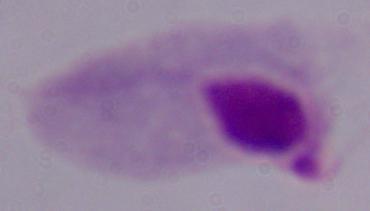
Summary:
  - Magnification: 1000x
  - Identification: trichomonad
  - Modality: micrograph